State the blood parasite species.
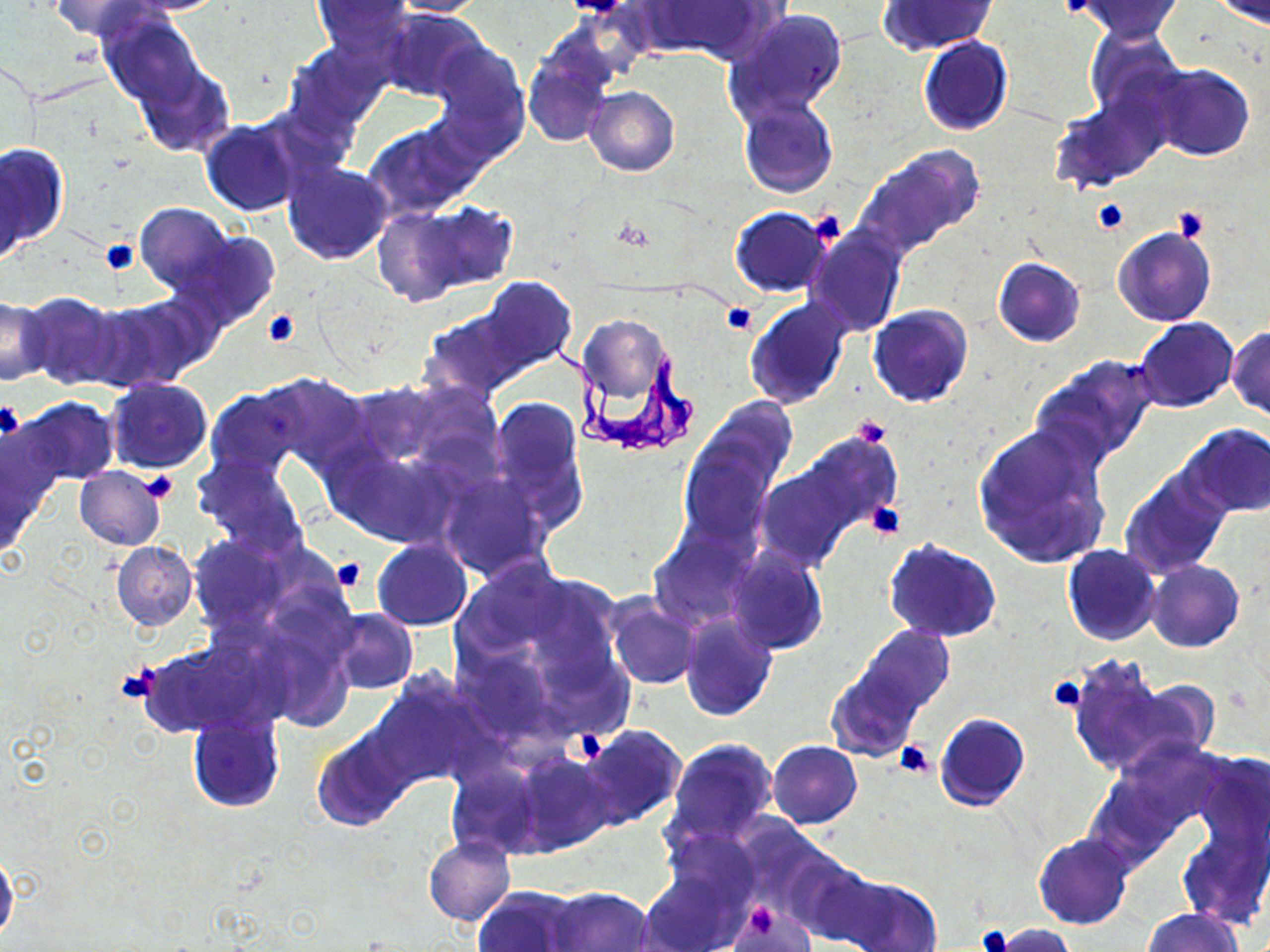
Trypanosoma brucei.

modality: light microscopy
preparation: thin blood smear
uninfected_red_blood_cell_locations: 'approximate bounding boxes as [x1, y1, x2, y2] in pixels: [51, 0, 158, 41], [123, 0, 230, 15], [311, 0, 415, 55], [387, 0, 487, 16], [640, 0, 773, 62], [1073, 0, 1183, 41], [877, 1, 998, 55], [1210, 1, 1270, 26], [378, 7, 484, 101], [725, 8, 851, 125], [98, 10, 204, 109], [1083, 29, 1186, 125], [918, 36, 1012, 136], [429, 39, 528, 154], [288, 41, 390, 131], [523, 52, 613, 147], [133, 63, 234, 158], [1146, 65, 1254, 162], [585, 86, 679, 176], [1050, 94, 1166, 191], [738, 97, 839, 198], [201, 120, 303, 217], [364, 120, 481, 219], [0, 143, 67, 254], [855, 144, 985, 259], [0, 159, 26, 267], [282, 160, 394, 264], [371, 202, 509, 305], [135, 203, 232, 296], [729, 207, 832, 297], [804, 222, 906, 336], [1113, 226, 1217, 327], [180, 232, 280, 331], [993, 257, 1085, 347], [425, 284, 572, 397], [23, 293, 125, 390], [744, 296, 853, 409], [0, 297, 50, 384], [91, 297, 211, 390], [868, 305, 973, 407], [580, 316, 669, 403], [1133, 318, 1238, 412], [1226, 326, 1270, 418], [1033, 355, 1159, 469], [257, 372, 369, 474], [106, 378, 212, 473], [346, 383, 442, 466], [206, 388, 303, 481], [487, 396, 587, 528], [19, 398, 118, 485], [689, 399, 795, 512], [972, 422, 1112, 570], [1180, 424, 1269, 517], [772, 430, 900, 552], [677, 433, 780, 550], [324, 443, 453, 547], [192, 454, 307, 557], [756, 466, 864, 570], [74, 467, 165, 551], [1119, 468, 1231, 579], [438, 474, 550, 580], [184, 533, 298, 633], [650, 533, 750, 628], [372, 539, 472, 630], [884, 539, 1001, 644], [112, 540, 197, 630], [1062, 546, 1162, 646], [726, 547, 828, 655], [1147, 561, 1244, 654], [607, 596, 702, 690], [327, 610, 416, 694], [678, 611, 777, 722], [857, 624, 954, 715], [458, 646, 556, 741], [1068, 658, 1189, 777], [828, 669, 921, 760], [369, 675, 485, 788], [934, 713, 1028, 811], [188, 718, 283, 811], [577, 724, 687, 831], [314, 730, 414, 831], [666, 738, 778, 844], [768, 740, 862, 829], [1188, 750, 1269, 858], [514, 752, 612, 854], [446, 760, 541, 858], [1180, 822, 1269, 929], [663, 827, 761, 913], [1034, 834, 1132, 930], [424, 837, 514, 926], [0, 850, 19, 944], [785, 857, 885, 947], [640, 869, 741, 952], [837, 877, 941, 952], [474, 887, 579, 952], [546, 887, 653, 952], [727, 902, 810, 950], [1142, 908, 1242, 952], [989, 923, 1075, 951]'
platelet_locations: 'approximate bounding boxes as [x1, y1, x2, y2] in pixels: [1091, 199, 1130, 235], [1173, 204, 1210, 244], [807, 210, 847, 249], [100, 238, 138, 275], [722, 303, 756, 334], [261, 309, 300, 347], [0, 403, 24, 441], [852, 414, 891, 448], [140, 471, 179, 504], [863, 501, 906, 541], [332, 558, 365, 593], [116, 663, 161, 703], [1049, 677, 1089, 713], [575, 732, 607, 763], [894, 740, 933, 778], [746, 903, 777, 940], [977, 925, 1011, 952]'
magnification: 1000x
image_size: 1270×952 pixels
stain: May-Grünwald-Giemsa
trypanosoma_brucei_locations: 'approximate bounding boxes as [x1, y1, x2, y2] in pixels: [544, 324, 697, 454]'
field_of_view: single